Classify this cell by malaria status.
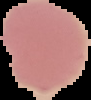
It is uninfected.

From a thin blood smear. Segmented cell region on a black background. Image is 91×100 pixels.